State which parasite is depicted.
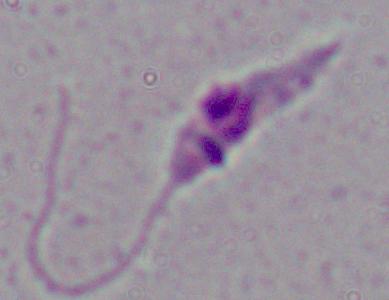

Leishmania.

modality = photomicrograph
magnification = 1000x